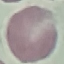
malaria status = uninfected
capture = smartphone through the microscope eyepiece
stain = Giemsa
image type = automatically extracted cell patch, resized to 64 × 64 pixels
preparation = thin blood film